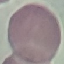
{
  "malaria_status": "uninfected",
  "stain": "Giemsa",
  "preparation": "thin blood film",
  "image_type": "cell patch, automatically extracted from a larger field of view and resized to 64 × 64 pixels",
  "capture": "smartphone through the microscope eyepiece"
}